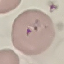

Summary:
  - Malaria status: parasitized
  - Capture: smartphone through the microscope eyepiece
  - Stain: Giemsa
  - Image type: automatically extracted cell patch, resized to 64 × 64 pixels
  - Preparation: thin blood smear